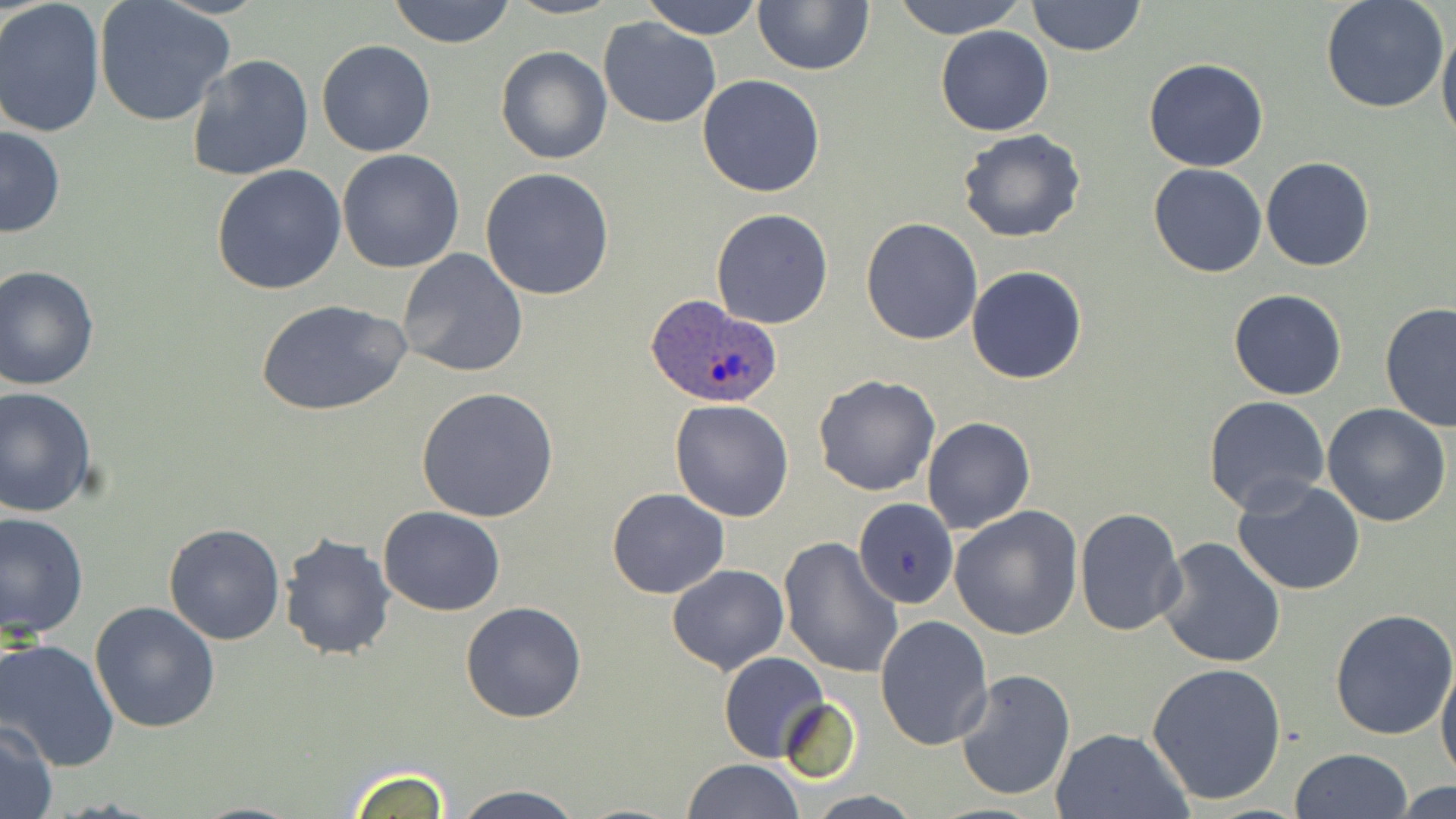

Summary:
  - Coordinate format: approximate bounding boxes as named x1/y1/x2/y2 corners in pixels
  - Plasmodium ovale-infected red blood cell locations: (x1=644, y1=294, x2=784, y2=408)
  - Uninfected red blood cell locations: (x1=389, y1=0, x2=516, y2=48), (x1=506, y1=0, x2=618, y2=19), (x1=642, y1=0, x2=762, y2=41), (x1=892, y1=0, x2=1026, y2=38), (x1=1027, y1=0, x2=1145, y2=57), (x1=0, y1=1, x2=106, y2=139), (x1=95, y1=1, x2=234, y2=127), (x1=753, y1=1, x2=874, y2=75), (x1=1320, y1=1, x2=1450, y2=113), (x1=598, y1=17, x2=722, y2=128), (x1=1437, y1=24, x2=1456, y2=148), (x1=935, y1=25, x2=1054, y2=136), (x1=316, y1=40, x2=435, y2=157), (x1=496, y1=47, x2=612, y2=164), (x1=183, y1=53, x2=314, y2=182), (x1=1144, y1=57, x2=1269, y2=171), (x1=696, y1=74, x2=826, y2=196), (x1=0, y1=123, x2=65, y2=239), (x1=957, y1=128, x2=1086, y2=244), (x1=337, y1=148, x2=465, y2=274), (x1=1261, y1=157, x2=1375, y2=271), (x1=1149, y1=163, x2=1267, y2=277), (x1=210, y1=165, x2=346, y2=296), (x1=480, y1=167, x2=616, y2=300), (x1=711, y1=208, x2=835, y2=329), (x1=860, y1=217, x2=983, y2=344), (x1=397, y1=248, x2=528, y2=379), (x1=966, y1=265, x2=1087, y2=383), (x1=0, y1=266, x2=100, y2=391), (x1=1229, y1=289, x2=1347, y2=400), (x1=257, y1=298, x2=412, y2=420), (x1=1379, y1=302, x2=1456, y2=431), (x1=813, y1=374, x2=941, y2=496), (x1=0, y1=386, x2=99, y2=518), (x1=415, y1=387, x2=559, y2=522), (x1=1203, y1=396, x2=1331, y2=515), (x1=669, y1=399, x2=795, y2=521), (x1=1322, y1=404, x2=1452, y2=529), (x1=921, y1=417, x2=1035, y2=536), (x1=1231, y1=477, x2=1366, y2=597), (x1=606, y1=487, x2=729, y2=598), (x1=853, y1=499, x2=958, y2=608), (x1=378, y1=505, x2=507, y2=616), (x1=948, y1=506, x2=1084, y2=641), (x1=1073, y1=507, x2=1186, y2=636), (x1=1, y1=510, x2=90, y2=640), (x1=162, y1=523, x2=286, y2=645), (x1=278, y1=532, x2=399, y2=662), (x1=778, y1=535, x2=903, y2=679), (x1=1156, y1=535, x2=1288, y2=668), (x1=667, y1=565, x2=789, y2=675), (x1=459, y1=600, x2=587, y2=723), (x1=89, y1=602, x2=222, y2=735), (x1=1329, y1=607, x2=1456, y2=741), (x1=875, y1=615, x2=994, y2=750), (x1=0, y1=638, x2=120, y2=771), (x1=719, y1=651, x2=829, y2=762), (x1=1436, y1=652, x2=1456, y2=785), (x1=1147, y1=662, x2=1289, y2=805), (x1=953, y1=666, x2=1076, y2=802), (x1=777, y1=697, x2=861, y2=782), (x1=0, y1=722, x2=58, y2=818), (x1=1049, y1=728, x2=1192, y2=819), (x1=1289, y1=748, x2=1416, y2=819), (x1=683, y1=758, x2=803, y2=819), (x1=346, y1=765, x2=454, y2=817), (x1=1391, y1=780, x2=1456, y2=818), (x1=451, y1=785, x2=588, y2=819), (x1=802, y1=792, x2=926, y2=819), (x1=188, y1=801, x2=309, y2=818)
  - Slide-level diagnosis: Plasmodium ovale
  - Preparation: thin blood smear
  - Stain: May-Grünwald-Giemsa
  - Image size: 1456×819 pixels
  - Magnification: 1000x
  - Field of view: single
  - Modality: optical microscopy